Assess for malaria.
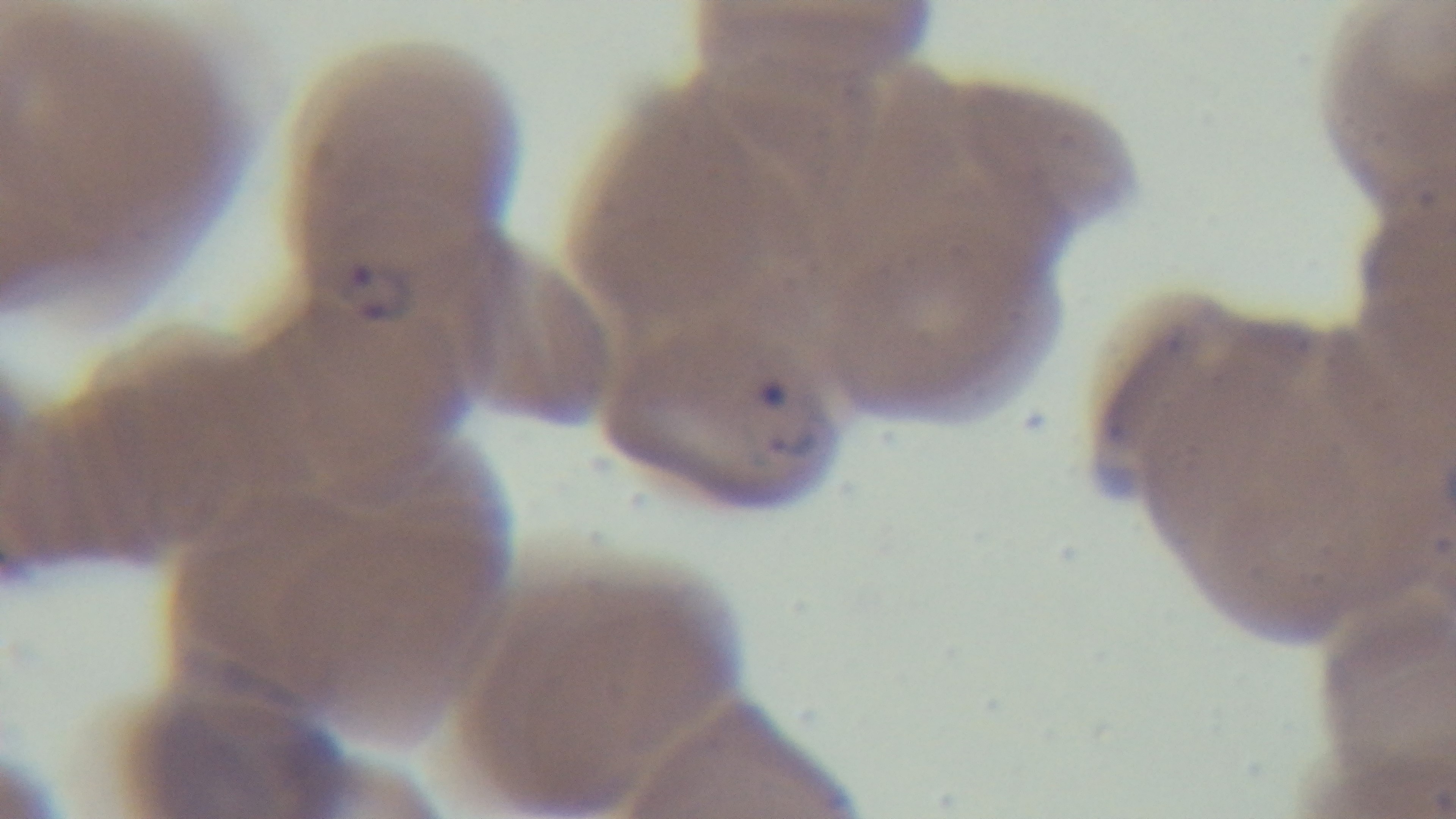

Infected.

Preparation: thin blood film. Captured with a mounted 4K digital camera. Light microscopy. Single field of view. 100x oil-immersion objective. Giemsa-stained.